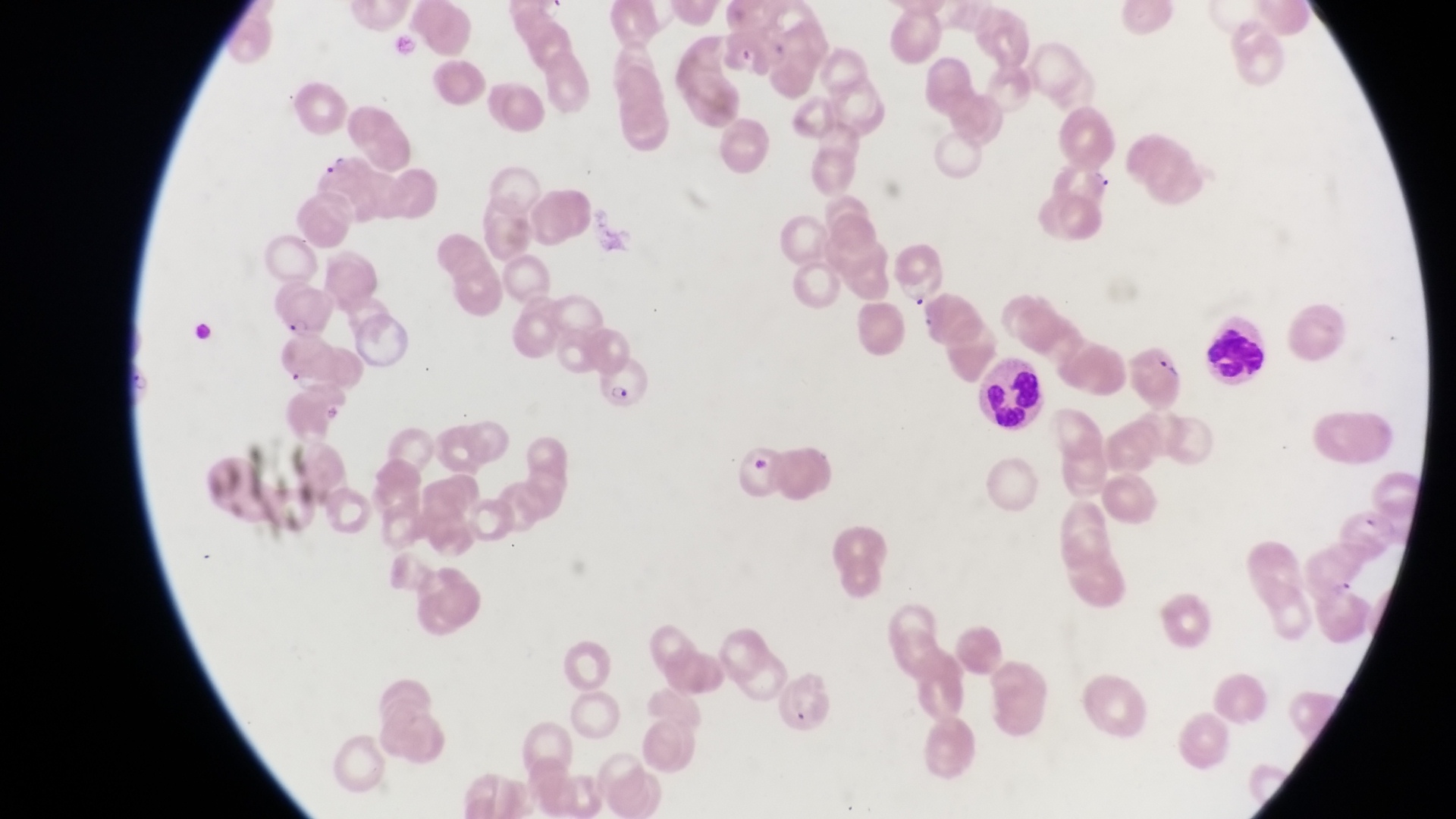

trophozoite locations = approximate bounding boxes as [left, top, right, bottom] in pixels: [1087, 164, 1116, 196]
parasitised red blood cell locations = approximate bounding boxes as [left, top, right, bottom] in pixels: [890, 248, 946, 308], [277, 284, 336, 333], [271, 338, 350, 393], [598, 353, 648, 417]
capture = smartphone photograph through the eyepiece of an Olympus CX-23 microscope
artifact (platelet-like body, stain precipitate, or debris) locations = approximate bounding boxes as [left, top, right, bottom] in pixels: [750, 457, 774, 474]
field of view = single
preparation = thin blood film
leukocyte locations = approximate bounding boxes as [left, top, right, bottom] in pixels: [1205, 312, 1269, 386], [978, 353, 1050, 432]
country = Uganda
magnification = 1000x
image size = 1456×819 pixels